Give the preparation type.
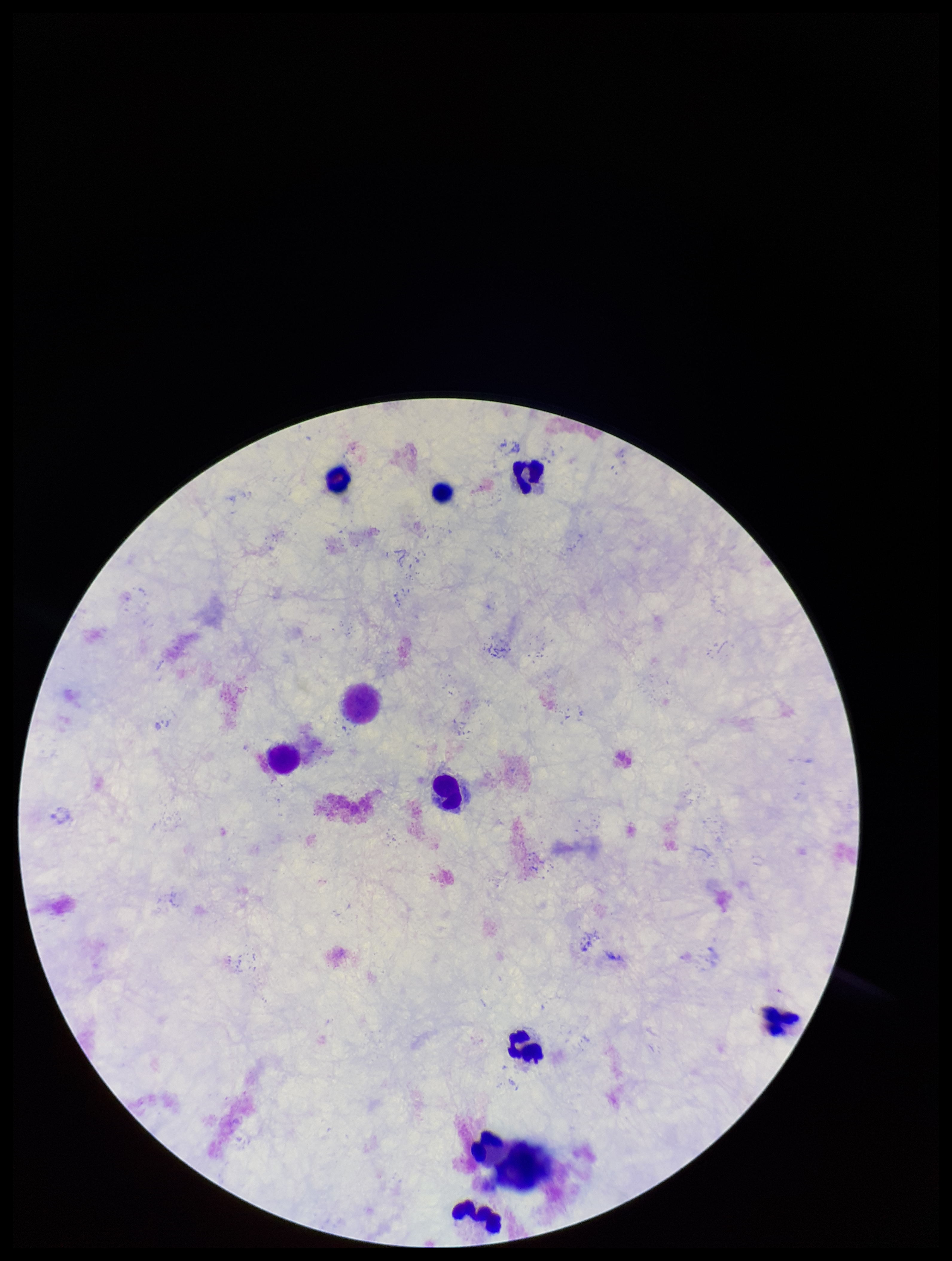
It is a thick blood smear.

Leukocyte count: 10. Parasite count: 0. Plasmodium parasites: none seen. Photographed through the microscope eyepiece with a smartphone camera. Image is 952×1261 pixels. Patient malaria status: negative. Single field of view. Stained with Giemsa.